Report the malaria status of this cell.
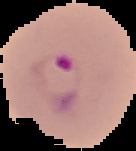

Parasitized.

From a thin blood smear. The area outside the segmented cell region is set to black. Image is 136×151 pixels.